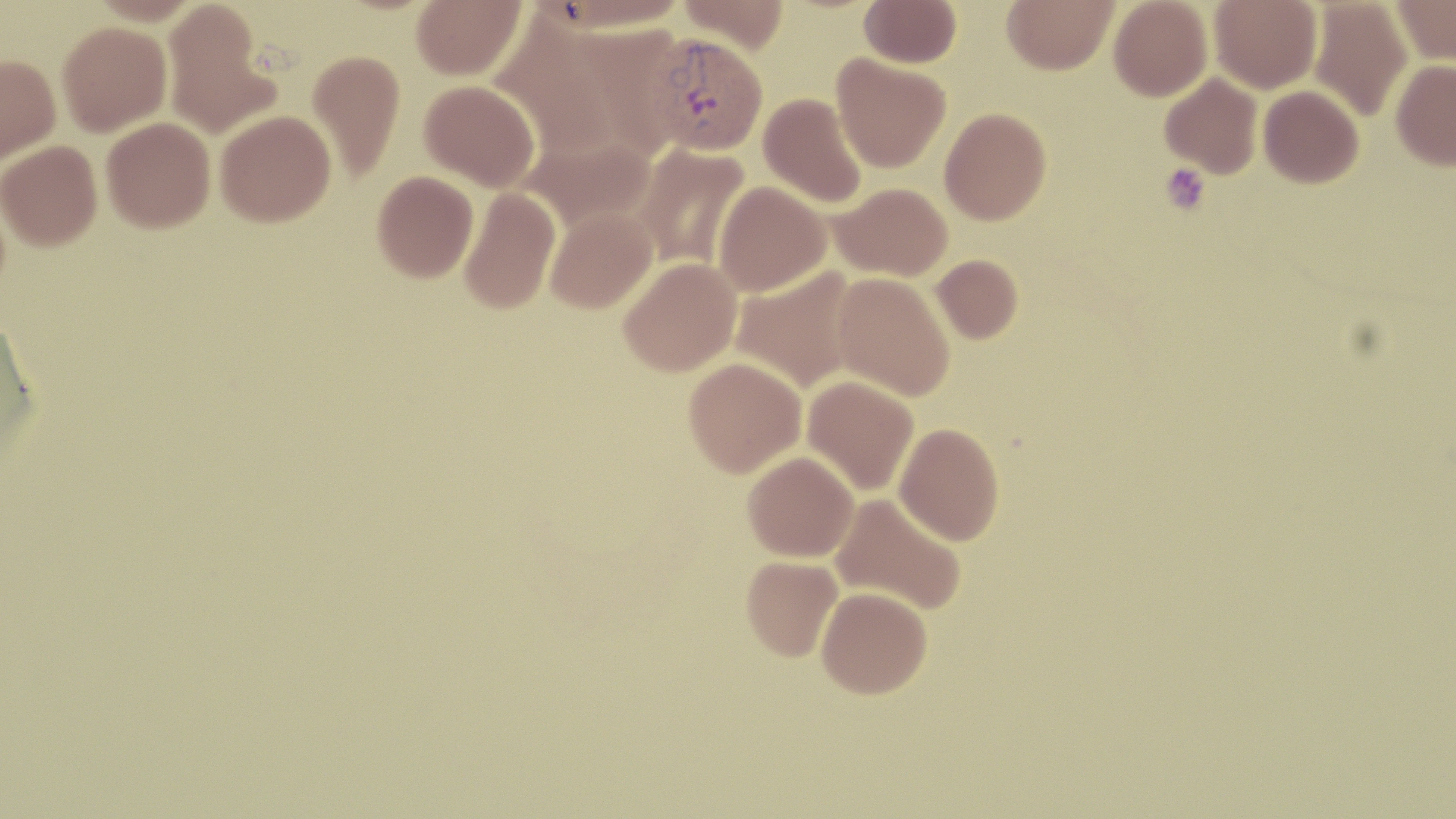
slide-level diagnosis = Plasmodium vivax
stain = May-Grünwald-Giemsa
magnification = 1000x
platelet locations = approximate bounding boxes as [x1, y1, x2, y2] in pixels: [1160, 163, 1211, 214]
field of view = single
modality = optical microscopy
Plasmodium vivax-infected red blood cell locations = approximate bounding boxes as [x1, y1, x2, y2] in pixels: [643, 33, 767, 156]
preparation = thin blood smear
uninfected red blood cell locations = approximate bounding boxes as [x1, y1, x2, y2] in pixels: [411, 0, 525, 80], [542, 0, 692, 33], [677, 0, 790, 53], [859, 0, 961, 68], [1002, 0, 1118, 75], [1108, 0, 1212, 101], [1209, 0, 1322, 94], [1308, 0, 1413, 121], [1392, 0, 1456, 66], [162, 1, 278, 140], [57, 21, 172, 137], [307, 49, 405, 183], [0, 54, 60, 166], [831, 54, 950, 173], [1391, 59, 1456, 171], [1159, 72, 1263, 179], [419, 80, 540, 191], [1258, 85, 1364, 188], [758, 92, 867, 209], [939, 107, 1051, 225], [215, 109, 336, 226], [101, 117, 215, 233], [519, 131, 660, 235], [0, 140, 102, 251], [632, 144, 751, 271], [372, 171, 478, 282], [713, 181, 831, 298], [828, 182, 952, 281], [459, 187, 561, 314], [544, 207, 657, 314], [931, 254, 1023, 344], [618, 257, 742, 376], [731, 266, 859, 393], [832, 272, 955, 401], [0, 315, 41, 460], [683, 357, 806, 477], [803, 376, 918, 496], [894, 422, 1004, 546], [742, 451, 859, 561], [830, 492, 968, 615], [741, 555, 843, 661], [816, 586, 932, 698]
image size = 1456×819 pixels